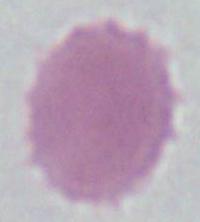

magnification = 1000x
identification = red blood cell
modality = photomicrograph